Assess this cell for malaria.
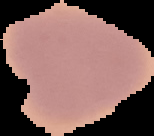
It is uninfected.

{
  "preparation": "thin blood film",
  "image_type": "cell region segmented out of the field of view; surrounding area masked to black",
  "image_size": "154×136 pixels"
}